Assess this cell for malaria.
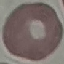

Uninfected.

Giemsa stain. Automatically extracted cell patch, resized to 64 × 64 pixels. Thin blood film. Acquired by smartphone through the microscope eyepiece.